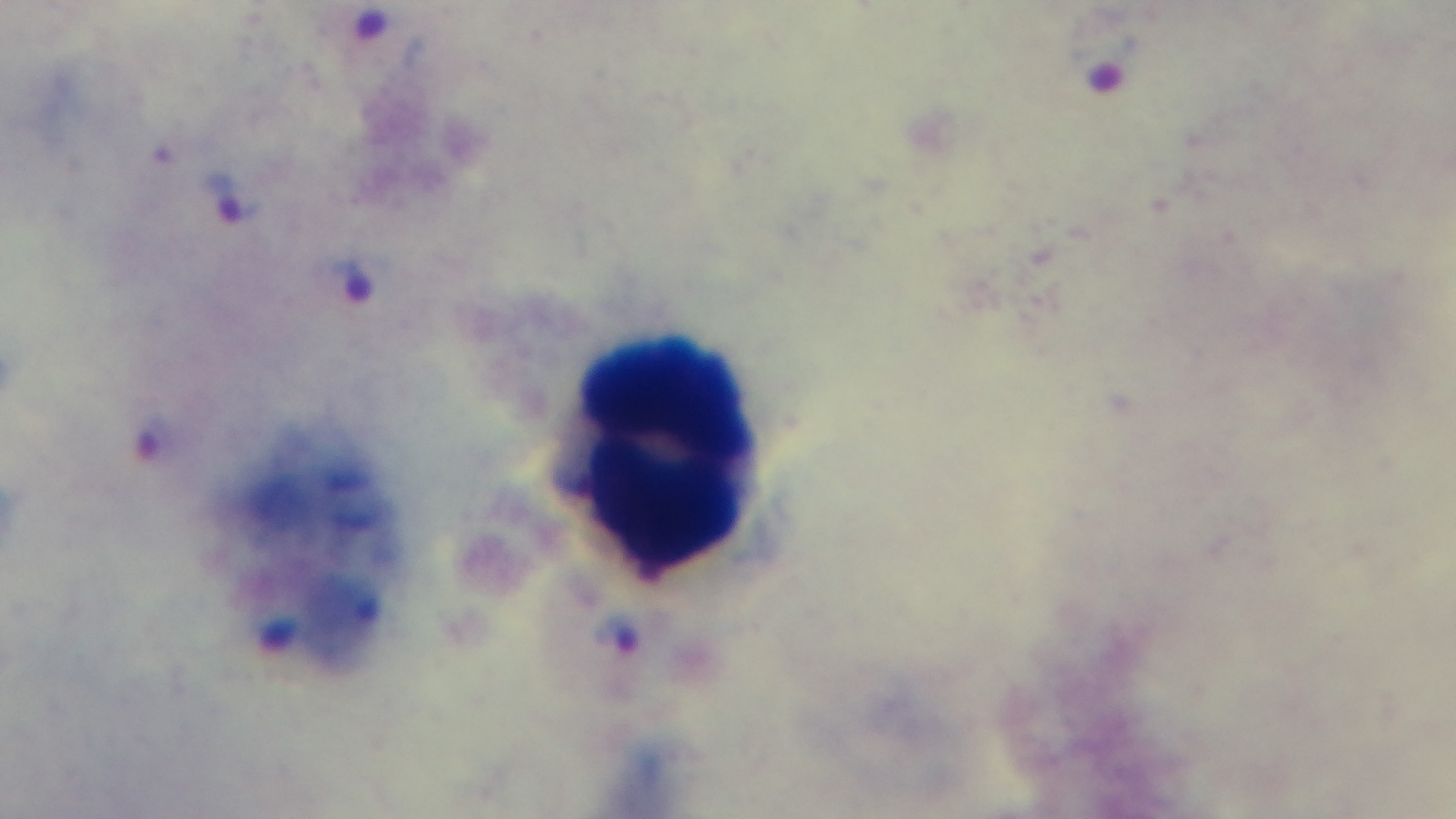
{
  "stain": "Giemsa",
  "malaria_status": "infected",
  "preparation": "thick smear",
  "capture": "mounted 4K digital camera",
  "modality": "light microscopy",
  "objective": "100x oil immersion",
  "field_of_view": "one from the slide"
}